Name the cell type shown.
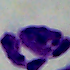

This is a leukocyte.

{
  "magnification": "1000x",
  "modality": "photomicrograph"
}